State which parasite is depicted.
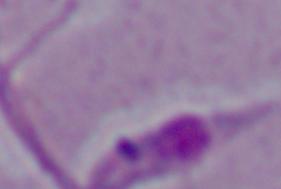

This is Leishmania.

Summary:
  - Modality: photomicrograph
  - Magnification: 1000x